Classify this cell by malaria status.
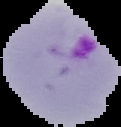

It is parasitized.

{
  "image_size": "121×127 pixels",
  "preparation": "thin blood film",
  "image_type": "segmented cell region on a black background"
}